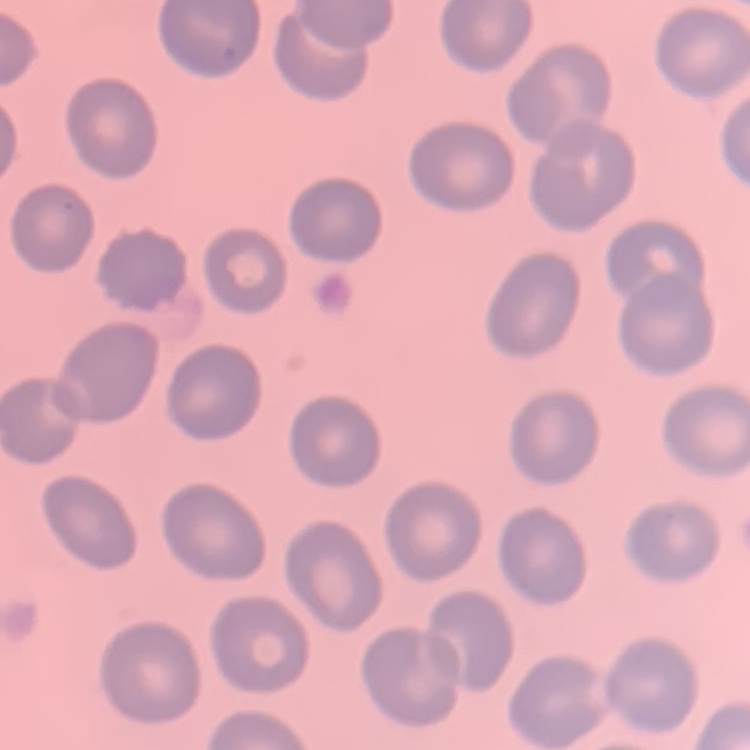

Summary:
  - Red blood cell morphology: no rouleaux formation
  - Preparation: thin blood film
  - Image type: square crop of a larger photomicrograph
  - Stain: Field's or Giemsa